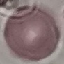

Summary:
  - Malaria status: uninfected
  - Capture: smartphone through the microscope eyepiece
  - Stain: Giemsa
  - Image type: cell patch, automatically extracted from a larger field of view and resized to 64 × 64 pixels
  - Preparation: thin smear